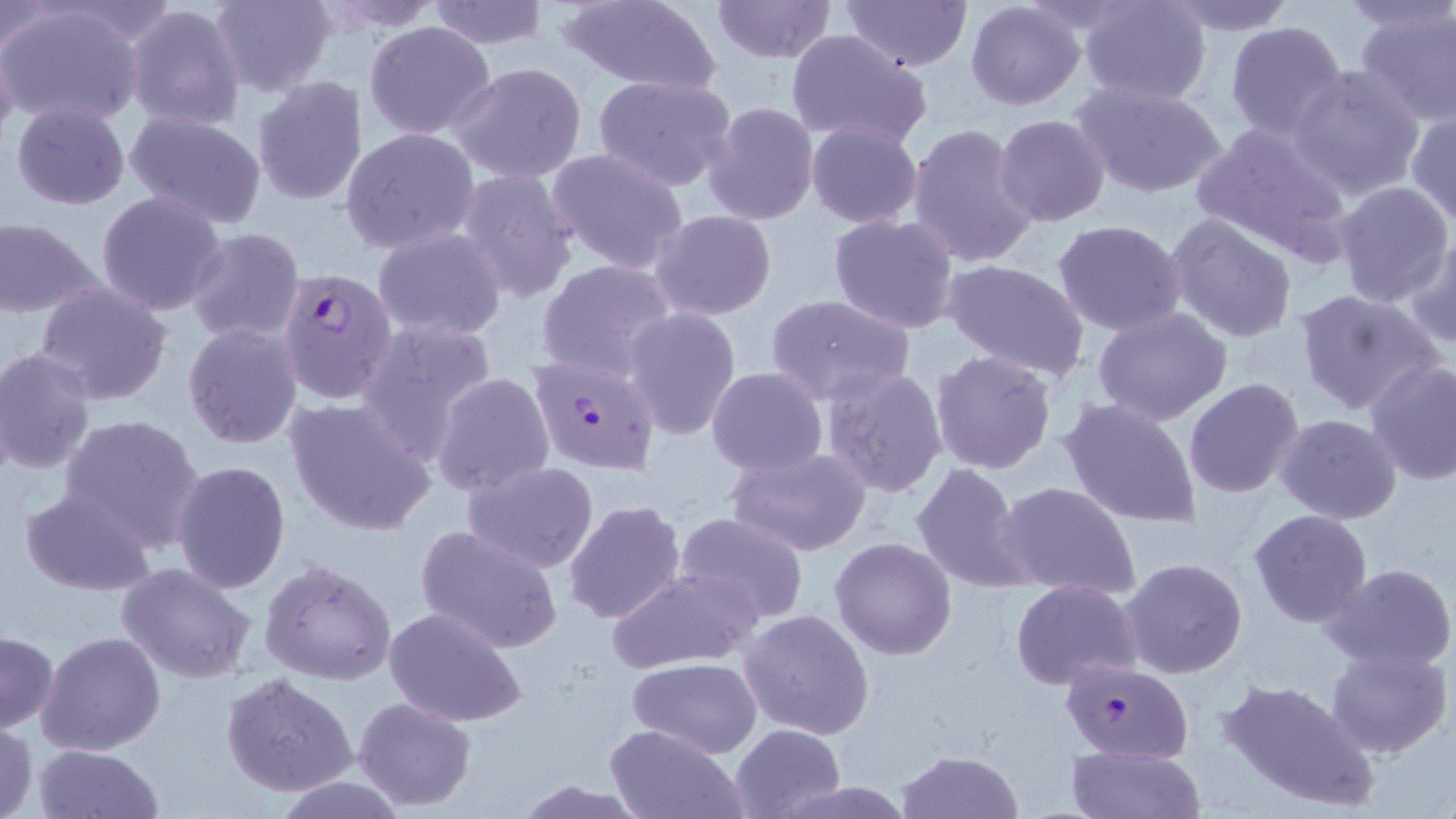

slide-level diagnosis = Plasmodium falciparum
preparation = thin blood film
field of view = one of a larger specimen
image size = 1456×819 pixels
stain = May-Grünwald-Giemsa
Plasmodium falciparum-infected red blood cell locations = approximate bounding boxes as [x1, y1, x2, y2] in pixels: [292, 269, 391, 393], [527, 353, 661, 475], [1059, 658, 1195, 762]
magnification = 1000x
uninfected red blood cell locations = approximate bounding boxes as [x1, y1, x2, y2] in pixels: [208, 0, 335, 95], [426, 0, 551, 49], [711, 0, 838, 66], [839, 0, 972, 71], [1080, 0, 1213, 105], [1160, 0, 1300, 33], [1338, 0, 1453, 35], [307, 1, 447, 33], [559, 1, 721, 91], [965, 1, 1086, 111], [126, 2, 247, 132], [0, 3, 58, 59], [0, 3, 145, 127], [1355, 4, 1456, 124], [363, 20, 496, 140], [1223, 20, 1349, 144], [784, 30, 933, 152], [0, 41, 19, 152], [448, 61, 589, 184], [1288, 64, 1426, 201], [593, 73, 738, 192], [251, 76, 370, 207], [1074, 82, 1227, 201], [702, 101, 818, 227], [11, 102, 131, 210], [1407, 108, 1456, 226], [123, 110, 267, 230], [993, 114, 1110, 226], [806, 121, 923, 229], [907, 123, 1039, 269], [1191, 123, 1353, 258], [340, 127, 480, 256], [547, 148, 690, 275], [455, 168, 582, 304], [1332, 180, 1453, 307], [96, 190, 229, 317], [647, 209, 777, 319], [829, 213, 961, 334], [1166, 213, 1298, 343], [0, 217, 101, 317], [1052, 218, 1188, 336], [374, 226, 507, 341], [184, 227, 305, 346], [1403, 234, 1456, 349], [535, 259, 676, 381], [941, 259, 1090, 382], [32, 280, 174, 406], [1295, 288, 1444, 418], [764, 292, 915, 405], [623, 307, 742, 440], [1093, 308, 1233, 427], [356, 319, 499, 457], [182, 323, 304, 450], [0, 349, 96, 476], [929, 349, 1059, 476], [1365, 360, 1456, 485], [819, 366, 949, 499], [706, 368, 827, 478], [431, 372, 556, 499], [1183, 378, 1305, 499], [1058, 396, 1204, 528], [285, 397, 439, 536], [59, 413, 205, 552], [1275, 413, 1403, 525], [726, 446, 874, 558], [171, 459, 291, 595], [462, 460, 600, 574], [910, 462, 1037, 595], [994, 481, 1140, 599], [19, 489, 155, 595], [562, 499, 688, 625], [1247, 509, 1373, 630], [672, 511, 808, 626], [415, 523, 562, 653], [830, 535, 958, 660], [261, 558, 396, 686], [1119, 558, 1248, 680], [115, 562, 259, 685], [1322, 562, 1456, 670], [604, 568, 759, 675], [1012, 579, 1142, 690], [383, 605, 526, 727], [739, 608, 875, 740], [1, 631, 58, 733], [36, 632, 167, 756], [1326, 648, 1453, 758], [628, 656, 763, 758], [219, 671, 359, 797], [1215, 675, 1381, 814], [352, 695, 478, 811], [603, 722, 745, 819], [0, 723, 38, 819], [729, 723, 844, 818], [32, 742, 162, 819], [1065, 744, 1206, 819], [896, 749, 1022, 819], [277, 775, 404, 817]
modality = light microscopy